Name the parasite shown.
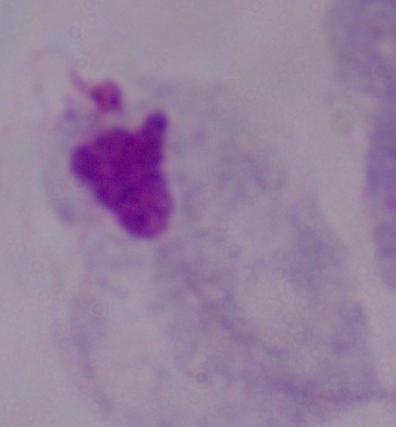

This is a trichomonad.

{
  "modality": "micrograph",
  "magnification": "1000x"
}